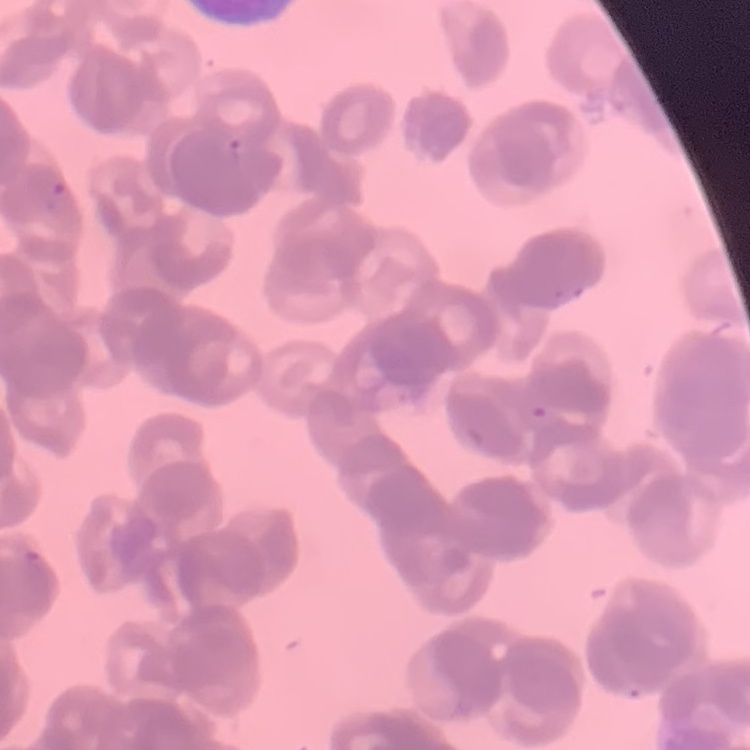

erythrocyte morphology = rouleaux formation
stain = Field's or Giemsa
preparation = thin blood smear
image type = square crop of a larger photomicrograph